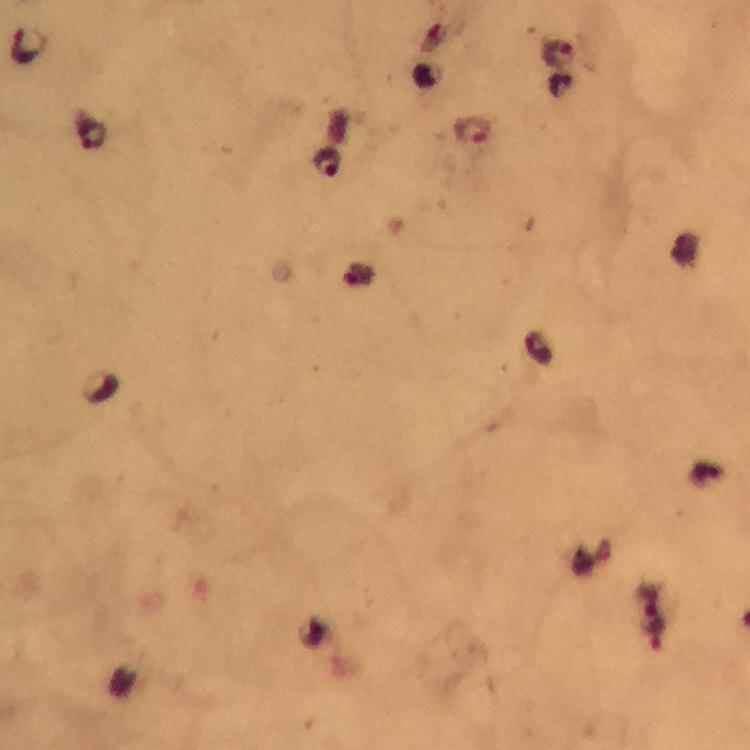
{
  "preparation": "thick smear",
  "malaria_parasite_locations": "approximate centers as [x, y] in pixels: [27, 44], [560, 55], [562, 85], [474, 131], [91, 134], [329, 164], [359, 276], [657, 635]",
  "capture": "smartphone mounted on the microscope",
  "cropped_from": "a single field of view",
  "context": "from a malaria diagnostic workup",
  "stain": "Giemsa",
  "image_size": "750×750 pixels",
  "magnification": "100x",
  "immersion_oil": "used"
}